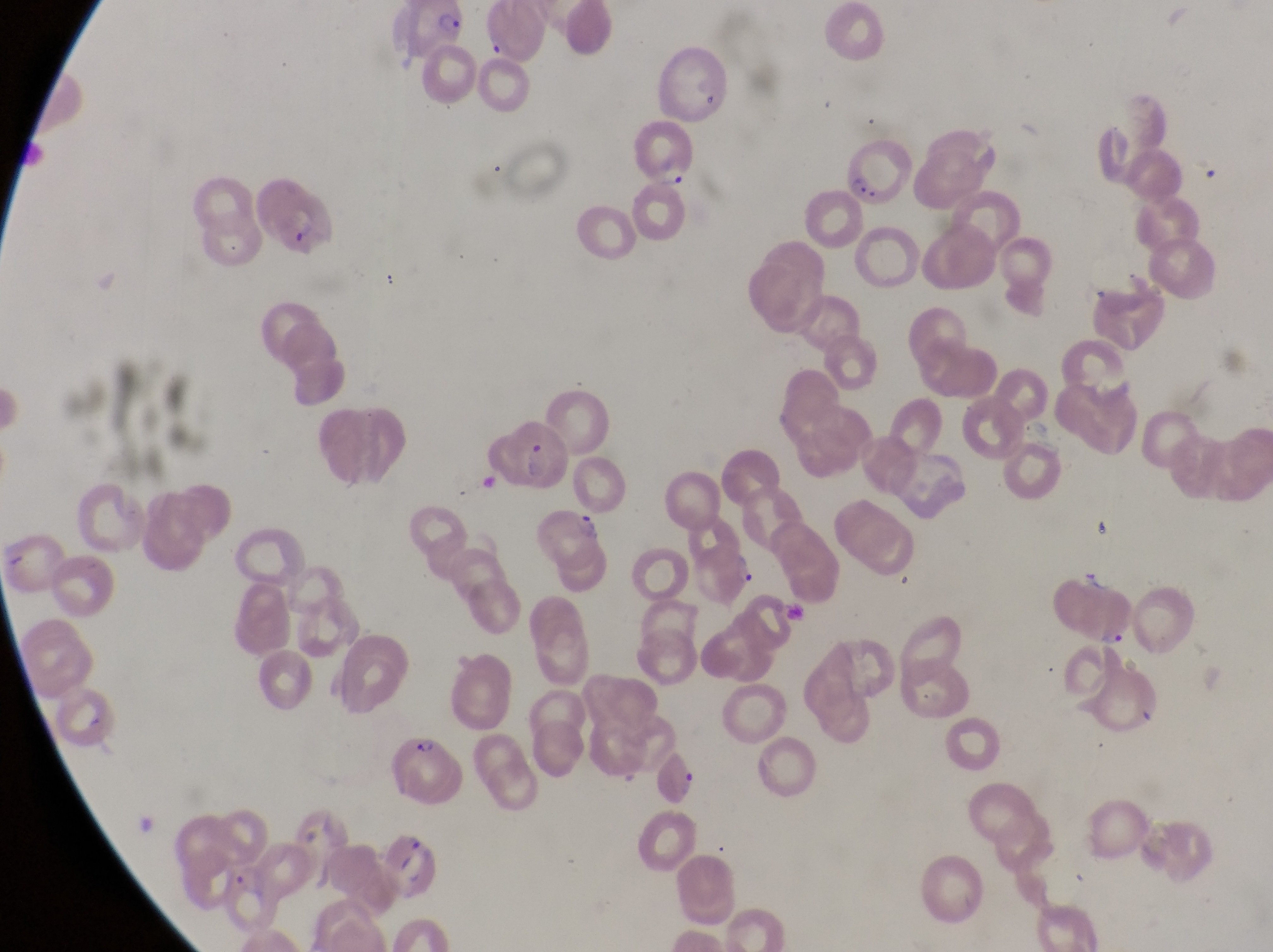 Approximate bounding boxes as [left, top, right, bottom] in pixels. Parasitised red blood cell locations: [385, 7, 468, 65], [656, 47, 731, 122], [627, 115, 702, 193], [843, 128, 917, 205], [255, 175, 342, 263], [505, 420, 577, 494], [535, 506, 610, 571], [694, 535, 757, 607], [1049, 565, 1137, 648], [392, 734, 469, 808], [659, 754, 697, 807], [385, 833, 445, 903], [220, 870, 286, 935]. Thin blood film. One field of view. At a magnification of 1000x. Sample from Uganda. Image is 1273×952 pixels. Captured by a smartphone held over the eyepiece of an Olympus CX-23 microscope.